Assess this cell for malaria.
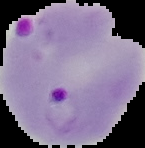

It is parasitized.

Segmented cell region on a black background. Image is 145×148 pixels. From a thin blood smear.